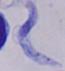
A trypanosome is seen. Captured at 1000x magnification. Micrograph.